Classify this cell by malaria status.
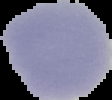
It is uninfected.

Segmented cell region on a black background. From a thin blood smear. Image is 112×100 pixels.